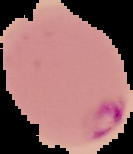

image type = segmented cell region on a black background
preparation = thin blood smear
malaria status = parasitized
image size = 133×154 pixels